Comment on the morphology of the erythrocytes.
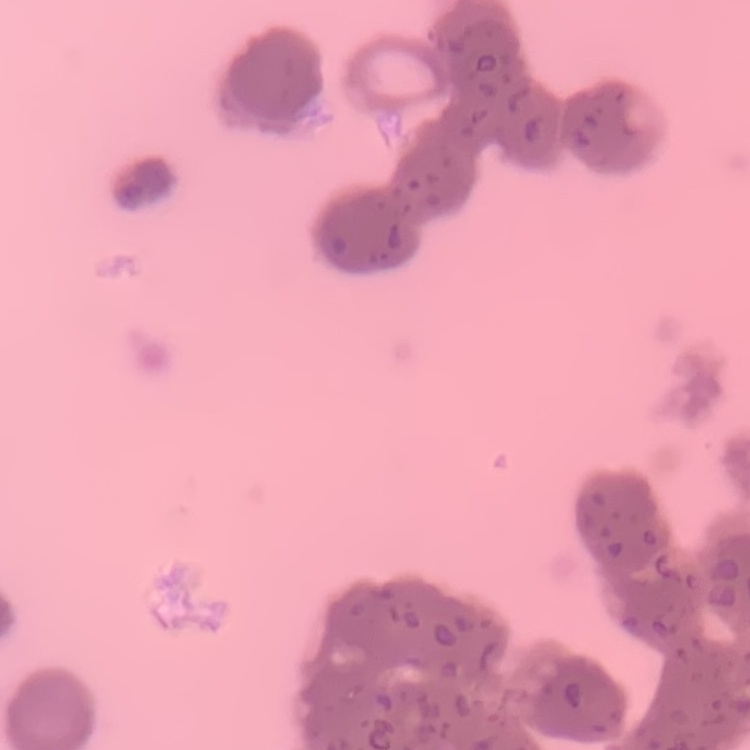
They show rouleaux formation.

Thin blood smear. One tile cut from a larger photomicrograph. Field's or Giemsa stain.